Locate malaria parasites and leukocytes.
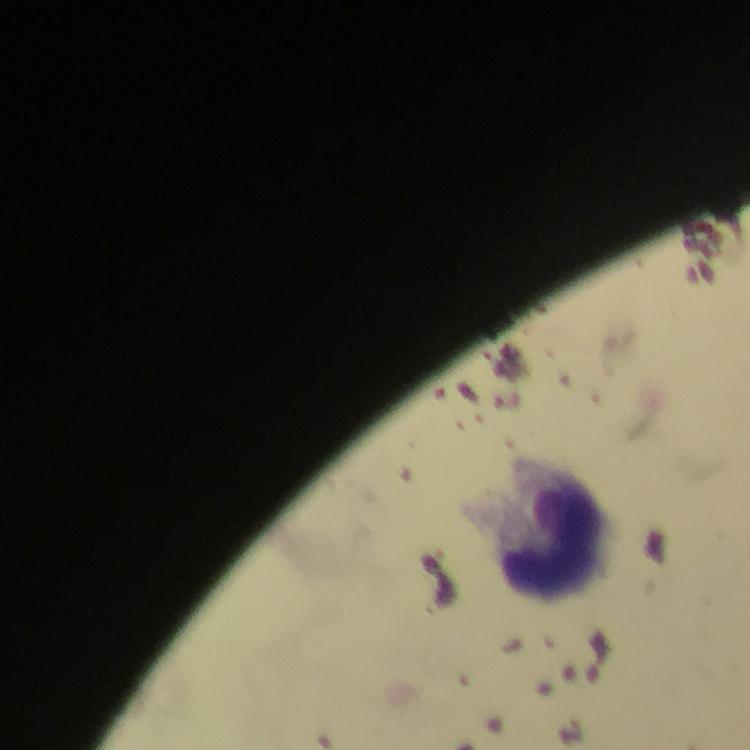

No malaria parasites seen.
Approximate object centers, in pixels from the top-left corner.
Leukocytes: (x=550, y=529).

Immersion oil was used. Giemsa-stained preparation. A crop from one field of view. Image is 750×750 pixels. From a malaria diagnostic workup. Thick blood film. Photographed through the microscope with a smartphone camera. At 100x magnification.